Name the parasite shown.
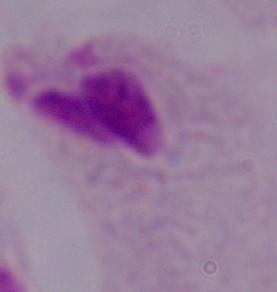

A trichomonad.

Captured at 1000x magnification. Micrograph.